Classify this cell by malaria status.
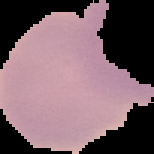
Uninfected.

Summary:
  - Image size: 154×154 pixels
  - Preparation: thin blood film
  - Image type: segmented cell region on a black background